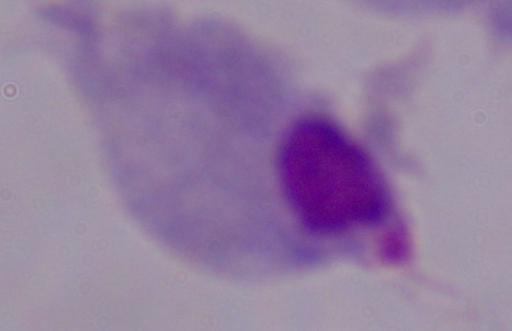

identification = trichomonad
modality = photomicrograph
magnification = 1000x